Locate leukocytes (white blood cells).
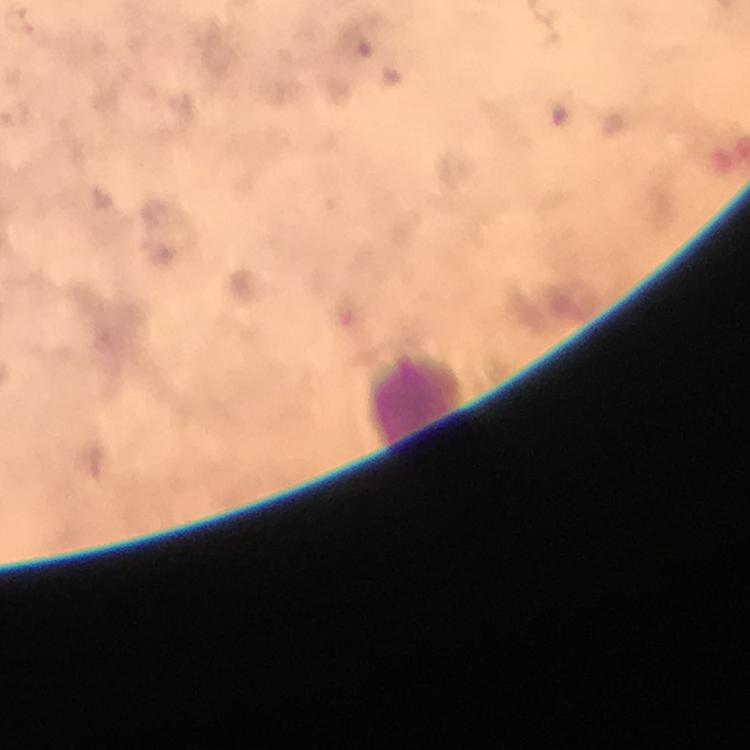
Approximate object centers, in pixels from the top-left corner.
Leukocytes: (x=414, y=400).

{
  "capture": "smartphone photograph through a microscope",
  "plasmodium_parasites": "none seen",
  "context": "from a diagnostic examination for malaria",
  "preparation": "thick blood smear",
  "stain": "Giemsa",
  "magnification": "100x",
  "cropped_from": "a single field of view",
  "image_size": "750×750 pixels",
  "immersion_oil": "used"
}